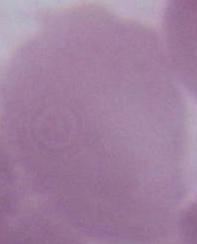
Summary:
  - Identification: erythrocyte
  - Magnification: 1000x
  - Modality: micrograph